Point out each Plasmodium parasite.
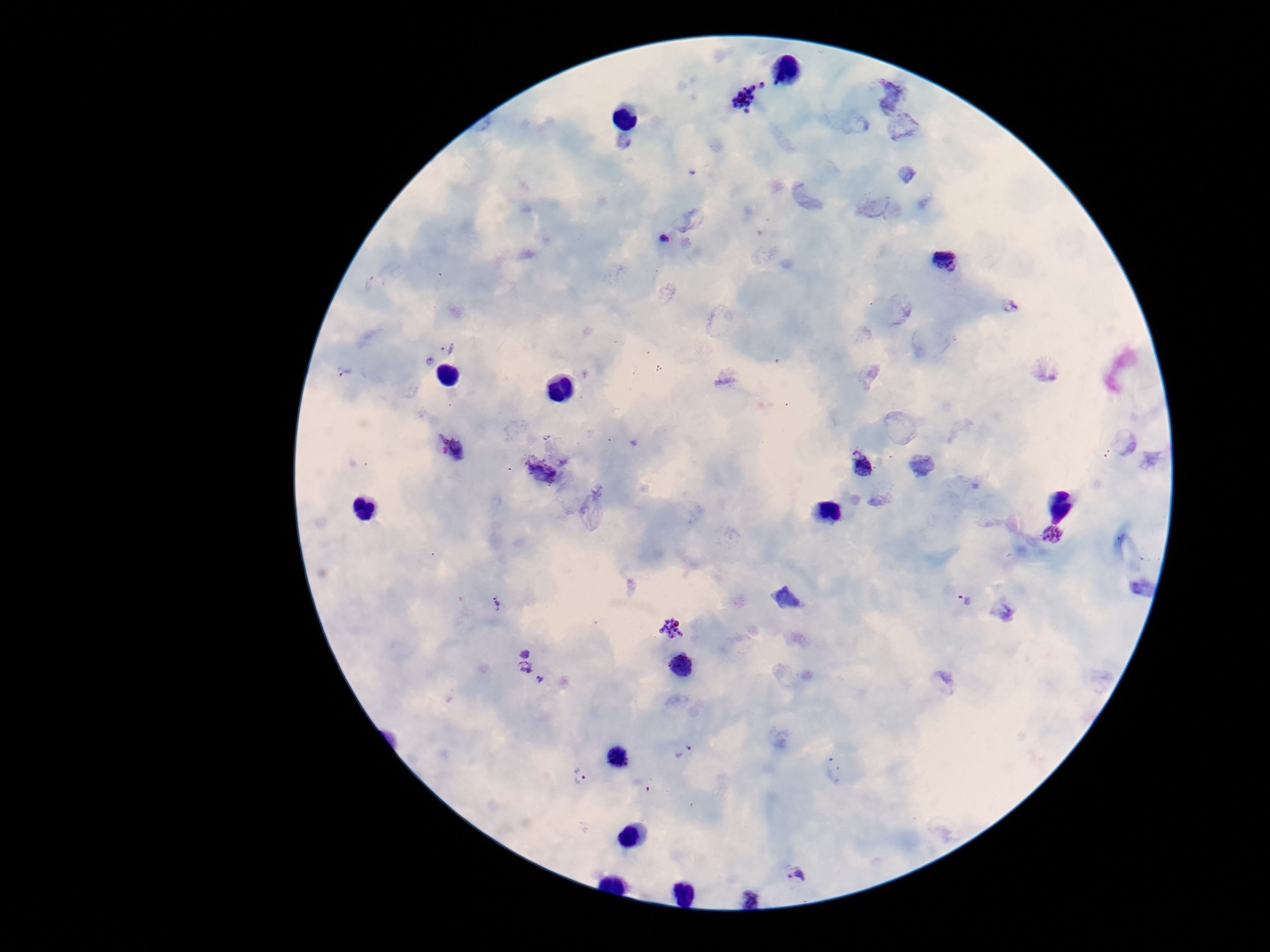
Approximate centers as (x, y) in pixels.
Plasmodium parasites: (751, 94), (891, 95), (904, 132), (665, 238), (945, 260), (1011, 307), (448, 347), (428, 361), (343, 371), (546, 436), (452, 447), (561, 456), (861, 464), (921, 465), (537, 471), (877, 497), (1053, 536), (786, 598), (967, 601), (496, 604), (1003, 609), (672, 628), (525, 651), (683, 666), (525, 667), (943, 682), (545, 683), (686, 751), (833, 768), (580, 778), (796, 872), (752, 899).

Summary:
  - Capture: smartphone camera through the microscope eyepiece
  - Preparation: thick blood film
  - Patient malaria status: positive
  - Image size: 1270×952 pixels
  - Field of view: single
  - Stain: Giemsa
  - Magnification: 100x